Give the extent of all Plasmodium ovale-infected red blood cells.
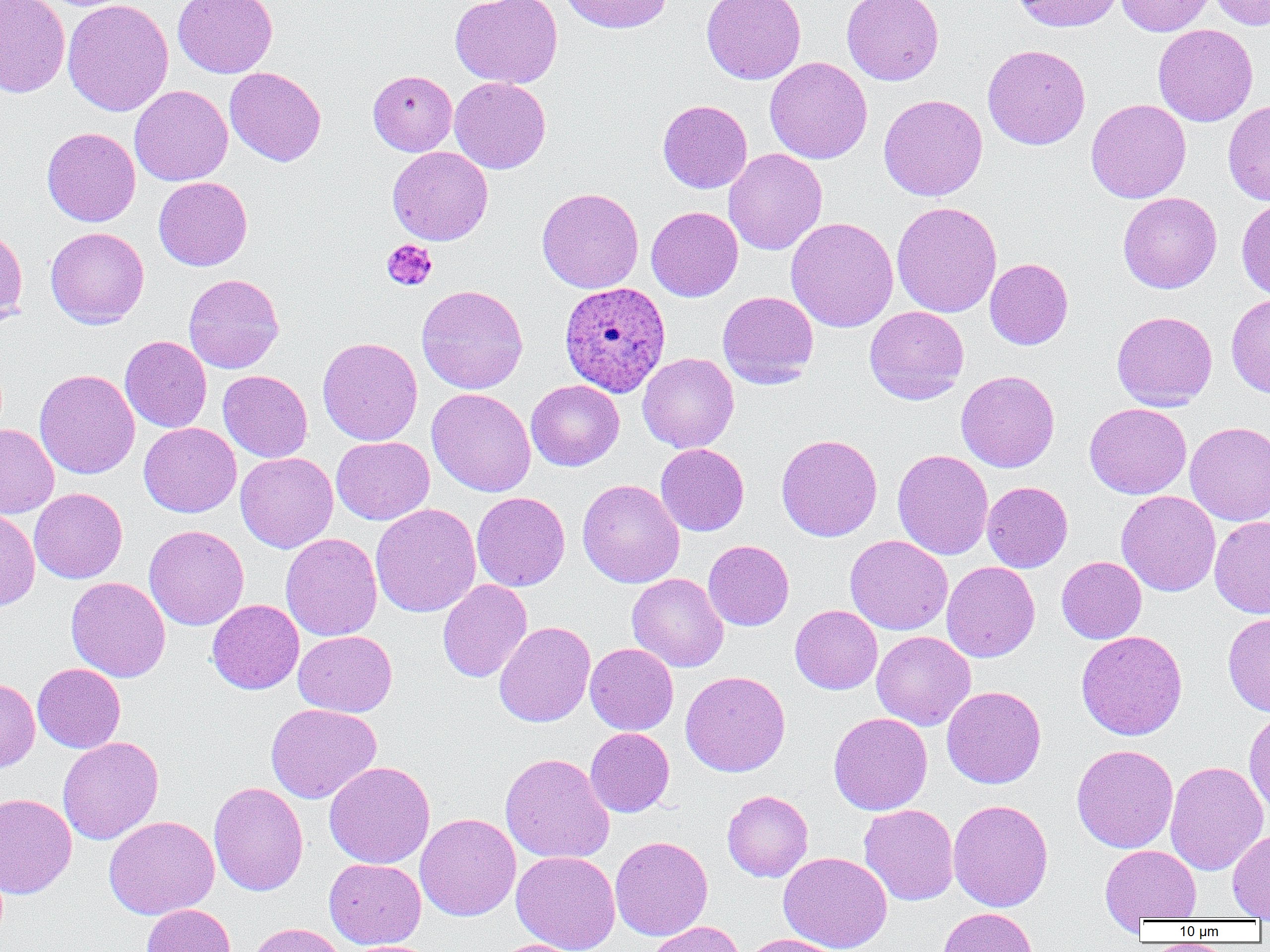
Approximate bounding boxes as (x1,y1)-(x2,y2) corner pairs in pixels.
Plasmodium ovale-infected red blood cells: (559,281)-(671,396).

Uninfected red blood cell locations: (0,0)-(70,98), (62,0)-(174,116), (172,0)-(278,78), (450,0)-(563,88), (560,0)-(672,33), (701,0)-(806,84), (842,0)-(944,85), (1013,0)-(1124,32), (1116,0)-(1216,36), (1209,0)-(1270,30), (1153,24)-(1257,126), (982,44)-(1091,150), (765,57)-(872,164), (224,67)-(326,166), (368,70)-(457,156), (450,77)-(551,173), (130,85)-(233,186), (878,94)-(987,201), (657,99)-(752,193), (1086,99)-(1191,203), (1223,99)-(1270,206), (42,127)-(140,227), (387,146)-(493,245), (724,148)-(827,255), (153,177)-(252,271), (536,187)-(644,293), (1118,192)-(1221,293), (891,201)-(1002,318), (646,206)-(743,301), (786,217)-(899,332), (0,224)-(28,327), (45,226)-(149,328), (984,258)-(1073,349), (184,273)-(284,373), (416,284)-(528,394), (718,291)-(819,388), (1226,293)-(1270,397), (864,306)-(969,404), (1112,311)-(1217,410), (120,335)-(212,433), (317,336)-(422,446), (637,352)-(739,453), (34,369)-(139,479), (218,370)-(312,462), (956,370)-(1059,472), (526,380)-(624,471), (427,388)-(537,497), (1084,403)-(1192,499), (1185,421)-(1270,525), (139,422)-(241,517), (0,424)-(59,519), (776,433)-(883,542), (331,436)-(434,525), (655,443)-(749,536), (893,449)-(994,560), (235,452)-(338,553), (577,479)-(684,588), (982,481)-(1073,572), (29,487)-(127,583), (1116,490)-(1221,596), (472,492)-(570,591), (370,503)-(481,618), (0,508)-(40,610), (1209,516)-(1270,619), (144,525)-(249,630), (281,533)-(383,641), (845,535)-(953,635), (703,540)-(794,630), (1056,556)-(1147,643), (942,561)-(1040,662), (627,573)-(729,672), (66,576)-(171,682), (437,579)-(533,682), (207,599)-(304,694), (790,605)-(882,694), (1222,612)-(1270,716), (494,621)-(595,728), (294,630)-(397,717), (1076,630)-(1188,740), (871,631)-(975,730), (585,643)-(679,735), (32,663)-(125,753), (680,670)-(791,777), (0,677)-(40,774), (941,685)-(1046,789), (266,703)-(381,804), (1243,707)-(1270,818), (828,712)-(932,815), (585,728)-(674,817), (57,737)-(163,844), (1072,744)-(1178,853), (500,752)-(615,864), (1165,760)-(1268,876), (324,761)-(435,869), (209,781)-(308,896), (722,790)-(813,881), (0,792)-(77,899), (948,799)-(1054,912), (859,804)-(959,905), (415,813)-(521,921), (103,815)-(219,920), (1227,827)-(1270,920), (610,836)-(713,941), (1101,845)-(1201,924), (511,851)-(620,952), (779,852)-(892,952), (324,858)-(426,950), (141,903)-(235,952), (937,907)-(1037,952), (644,920)-(746,952), (246,922)-(347,952), (740,934)-(846,952), (491,938)-(588,952). Platelet locations: (382,239)-(437,291). Slide-level diagnosis: Plasmodium ovale. Thin blood film. 1000x magnification. Image is 1270×952 pixels. Optical microscopy. Single field of view.